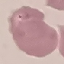

Malaria status: parasitized. Photographed with a smartphone camera at the microscope eyepiece. Cell patch, automatically extracted from a larger field of view and resized to 64 × 64 pixels. Thin blood film. Giemsa stain.